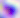 400x magnification. Toxoplasma gondii is seen. Photomicrograph.